Comment on the morphology of the red blood cells.
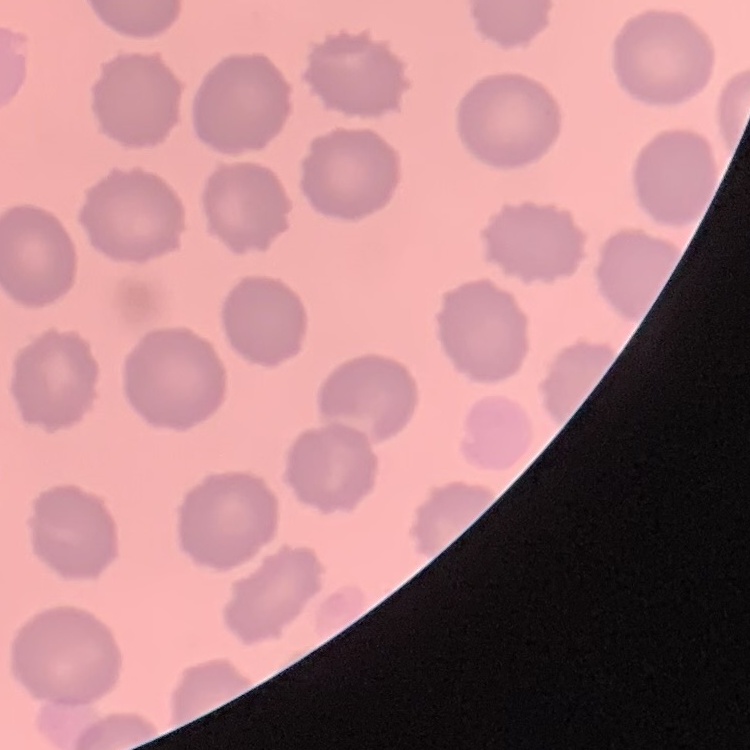

No rouleaux formation.

preparation = thin blood smear
image type = square crop of a larger photomicrograph
stain = Field's or Giemsa